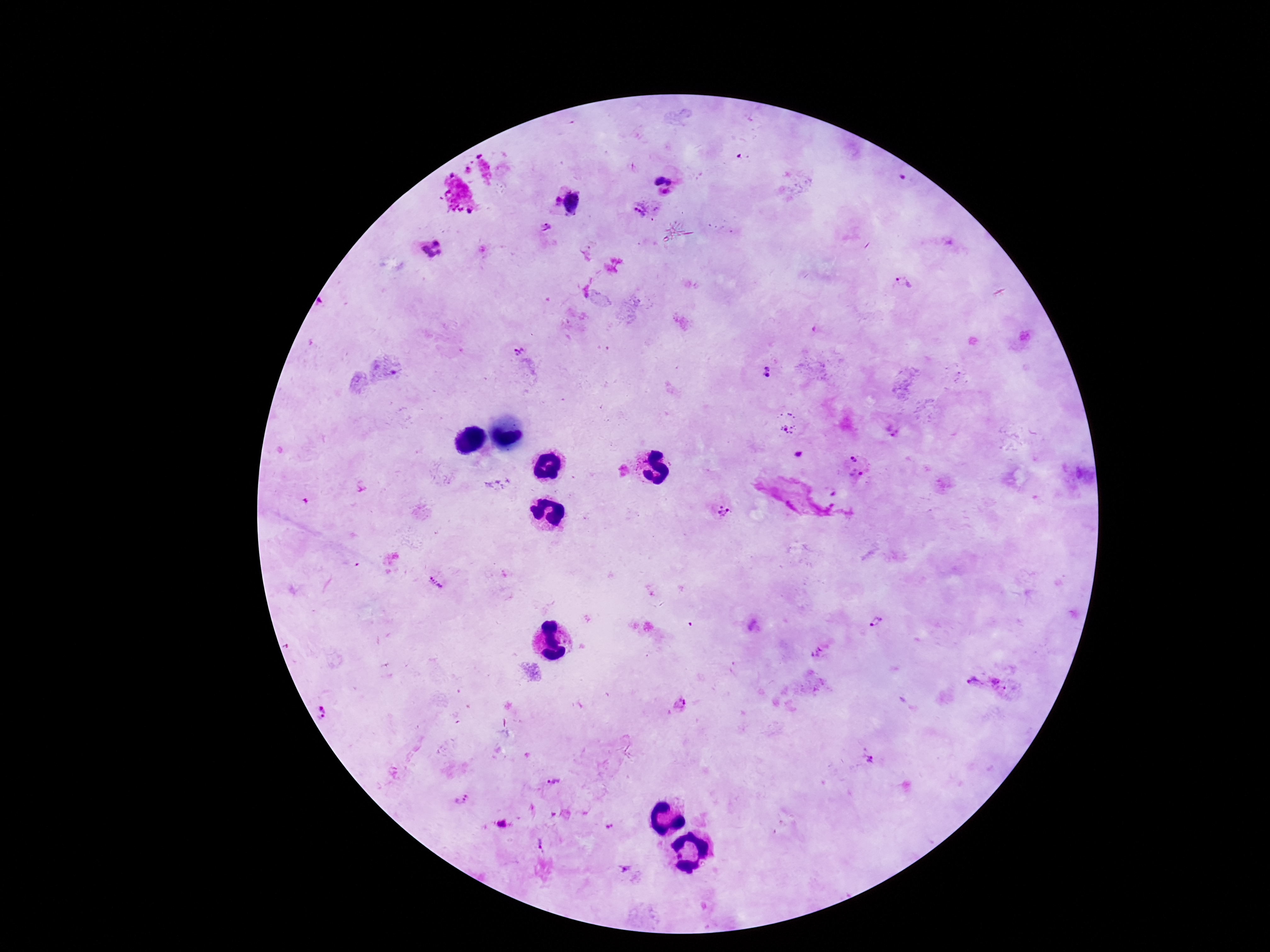

image size = 1270×952 pixels
stain = Giemsa
capture = smartphone camera through the microscope eyepiece
magnification = 100x
patient malaria status = positive
preparation = thick blood smear
Plasmodium parasite locations = approximate object centers, in pixels from the top-left corner: (x=664, y=183), (x=568, y=200), (x=640, y=211), (x=546, y=227), (x=431, y=248), (x=905, y=282), (x=517, y=352), (x=767, y=372), (x=787, y=421), (x=798, y=454), (x=855, y=458), (x=860, y=474), (x=497, y=483), (x=724, y=511), (x=435, y=581), (x=876, y=621), (x=819, y=652), (x=972, y=682), (x=1000, y=684), (x=322, y=711), (x=868, y=760), (x=555, y=783), (x=461, y=799), (x=503, y=824), (x=626, y=869)
field of view = single